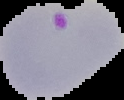
Summary:
  - Result: malaria parasites detected
  - Image type: cell region segmented out of the field of view; surrounding area masked to black
  - Preparation: thin blood film
  - Image size: 124×100 pixels